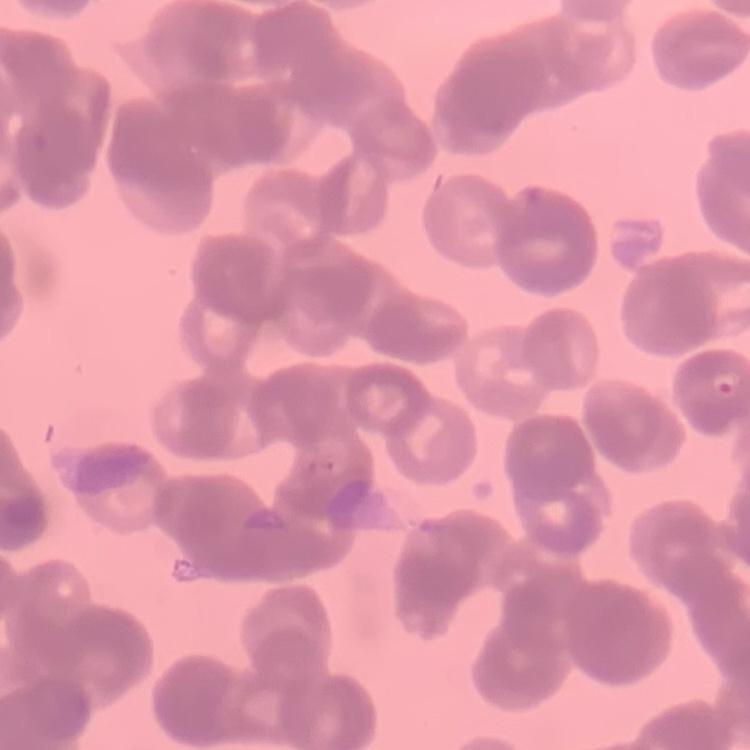

Summary:
  - Red blood cell morphology: rouleaux formation
  - Preparation: thin peripheral smear
  - Image type: one tile cut from a larger photomicrograph
  - Stain: Field's or Giemsa